State which parasite is depicted.
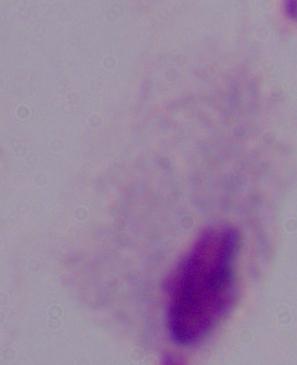

A trichomonad.

Summary:
  - Magnification: 1000x
  - Modality: micrograph